State which cell type is depicted.
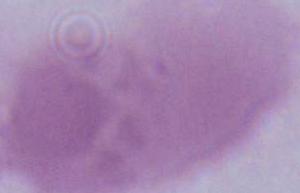
An erythrocyte.

1000x magnification. Photomicrograph.